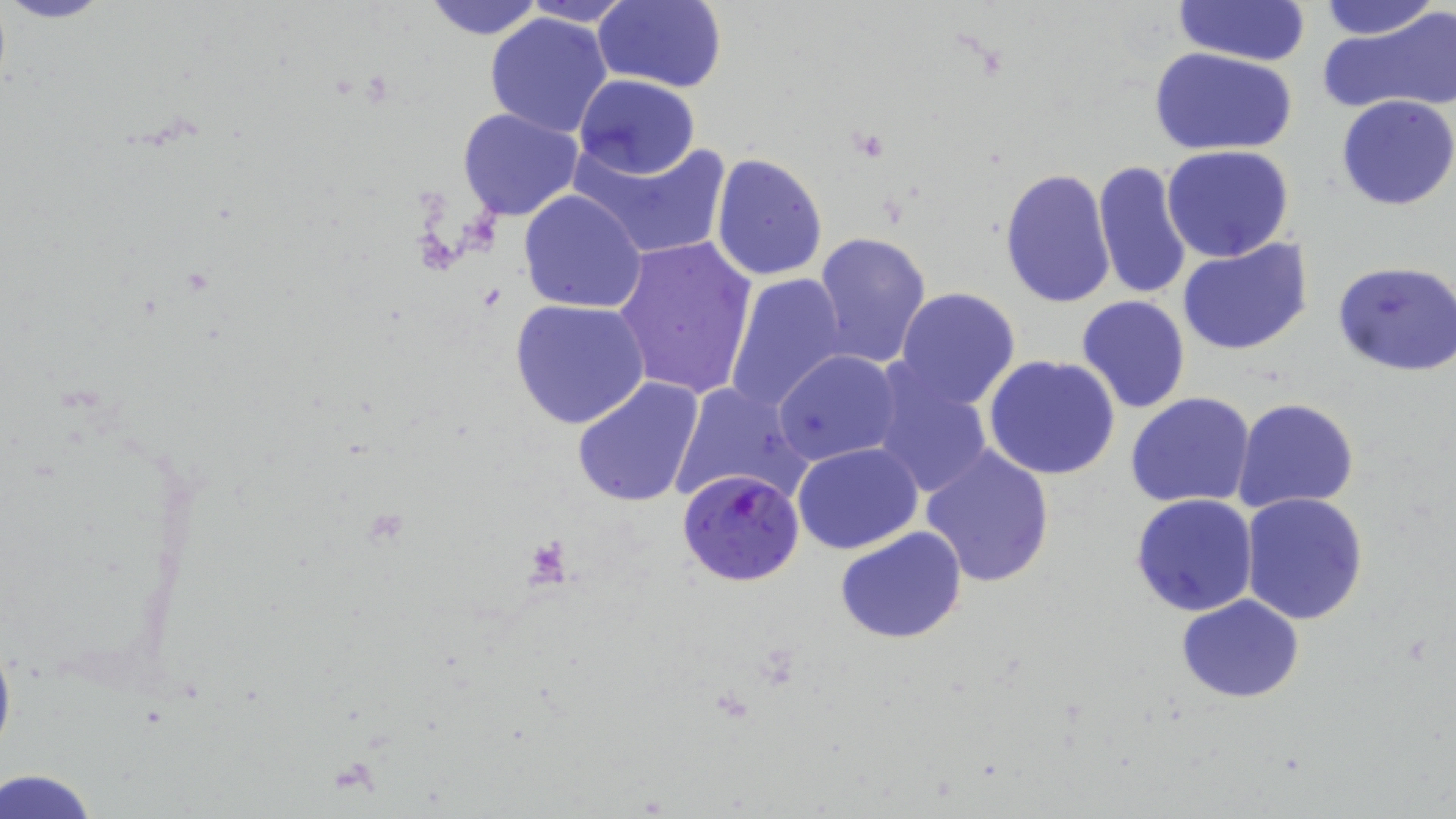

Summary:
  - Coordinate format: approximate bounding boxes as (x1, y1, x2, y2) in pixels
  - Plasmodium falciparum-infected red blood cell locations: (674, 467, 804, 589)
  - Uninfected red blood cell locations: (420, 0, 547, 40), (593, 0, 728, 92), (1172, 0, 1312, 66), (1319, 0, 1440, 41), (519, 1, 638, 26), (482, 11, 615, 139), (1318, 12, 1456, 116), (1149, 48, 1298, 156), (573, 74, 699, 180), (1336, 95, 1456, 211), (457, 107, 583, 223), (569, 136, 731, 260), (1162, 145, 1294, 263), (711, 152, 828, 282), (1094, 160, 1193, 301), (1000, 166, 1116, 308), (518, 189, 648, 313), (813, 231, 933, 366), (613, 234, 757, 401), (1177, 238, 1314, 355), (1334, 260, 1456, 375), (725, 272, 848, 412), (895, 286, 1021, 408), (1076, 295, 1192, 414), (510, 299, 652, 431), (773, 349, 901, 466), (984, 355, 1122, 481), (866, 364, 995, 499), (571, 377, 705, 508), (667, 380, 813, 506), (1125, 392, 1256, 510), (1233, 397, 1360, 514), (792, 441, 923, 554), (917, 444, 1057, 589), (802, 467, 945, 607), (1130, 493, 1259, 617), (1240, 493, 1369, 626), (834, 526, 968, 644), (1176, 594, 1305, 704), (2, 768, 100, 819)
  - Slide-level diagnosis: Plasmodium falciparum
  - Image size: 1456×819 pixels
  - Preparation: thin blood smear
  - Field of view: single
  - Modality: light microscopy
  - Magnification: 1000x
  - Stain: May-Grünwald-Giemsa